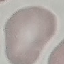
malaria_status: uninfected
image_type: cell patch, automatically extracted from a larger field of view and resized to 64 × 64 pixels
preparation: thin smear
capture: smartphone camera at the microscope eyepiece
stain: Giemsa